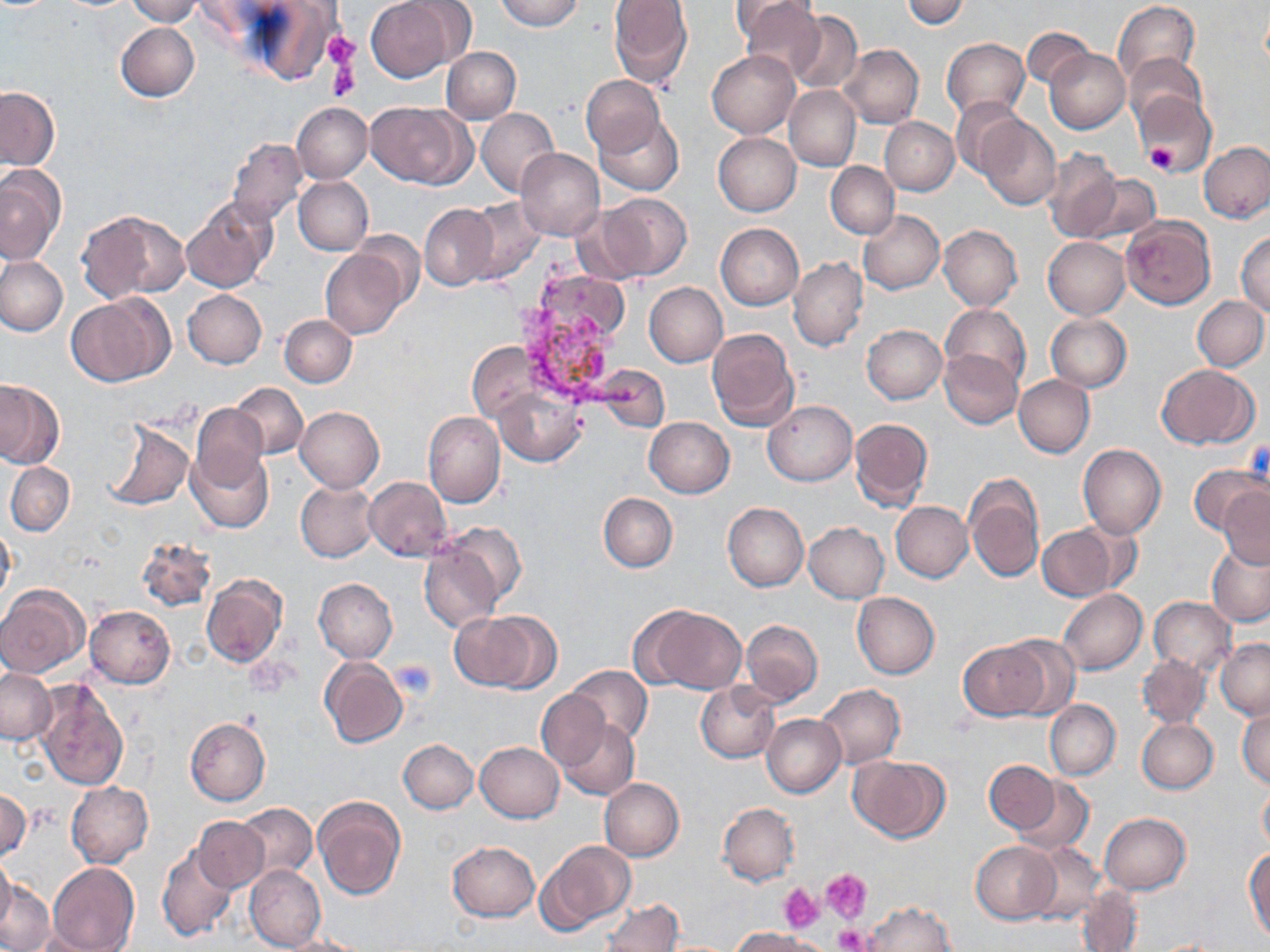

Summary:
  - Coordinate format: approximate bounding boxes as [x1, y1, x2, y2] in pixels
  - Platelet locations: [322, 32, 358, 70], [326, 52, 361, 102], [1146, 140, 1177, 175], [391, 661, 437, 699], [820, 869, 871, 923], [780, 883, 824, 933], [835, 925, 871, 952]
  - Uninfected red blood cell locations: [127, 0, 200, 26], [369, 0, 461, 81], [496, 0, 584, 31], [608, 0, 694, 88], [899, 0, 970, 29], [737, 1, 825, 82], [1113, 1, 1200, 86], [243, 2, 340, 86], [788, 9, 863, 94], [116, 22, 198, 101], [1021, 29, 1093, 89], [942, 37, 1029, 119], [839, 44, 924, 128], [441, 47, 520, 123], [1045, 49, 1129, 133], [707, 50, 798, 139], [1124, 54, 1206, 131], [581, 76, 664, 155], [784, 85, 861, 172], [0, 88, 58, 169], [1132, 92, 1215, 177], [952, 96, 1025, 178], [292, 102, 371, 183], [366, 102, 469, 188], [476, 107, 560, 197], [595, 115, 683, 197], [978, 116, 1060, 210], [880, 117, 958, 195], [714, 133, 801, 217], [226, 137, 307, 227], [1198, 141, 1270, 224], [516, 148, 605, 242], [1041, 150, 1123, 242], [826, 162, 899, 239], [830, 162, 928, 286], [0, 164, 66, 264], [1078, 172, 1161, 244], [294, 177, 373, 255], [598, 193, 692, 280], [182, 196, 277, 293], [464, 198, 547, 283], [420, 204, 500, 291], [858, 210, 944, 294], [79, 211, 189, 301], [1120, 215, 1215, 309], [715, 223, 804, 310], [938, 224, 1022, 311], [1236, 229, 1270, 316], [1042, 237, 1131, 318], [321, 248, 409, 339], [0, 256, 67, 335], [788, 257, 868, 351], [644, 282, 727, 366], [184, 290, 266, 368], [66, 294, 170, 386], [1193, 295, 1269, 371], [941, 304, 1030, 388], [1045, 314, 1131, 391], [279, 315, 356, 387], [862, 324, 947, 404], [707, 327, 799, 430], [469, 343, 537, 420], [938, 349, 1022, 428], [591, 362, 674, 434], [1158, 365, 1257, 448], [1013, 375, 1094, 458], [0, 378, 64, 468], [232, 382, 308, 459], [495, 387, 585, 467], [764, 401, 857, 485], [191, 403, 268, 488], [295, 406, 384, 494], [424, 412, 505, 508], [644, 416, 734, 497], [850, 418, 932, 510], [102, 419, 193, 511], [1079, 444, 1166, 539], [187, 447, 274, 532], [5, 462, 74, 536], [1189, 464, 1267, 536], [963, 473, 1044, 582], [364, 477, 452, 562], [296, 480, 379, 562], [1219, 488, 1270, 569], [599, 493, 677, 572], [723, 502, 808, 591], [891, 502, 972, 582], [0, 521, 14, 609], [444, 521, 524, 603], [804, 522, 888, 602], [1038, 524, 1120, 602], [136, 536, 215, 612], [419, 539, 506, 632], [1207, 542, 1270, 627], [201, 575, 287, 669], [314, 578, 397, 663], [0, 587, 87, 677], [1058, 589, 1147, 674], [852, 592, 939, 679], [1149, 597, 1235, 672], [86, 606, 175, 688], [639, 606, 748, 695], [463, 610, 561, 695], [740, 620, 823, 706], [1002, 637, 1079, 716], [1217, 639, 1270, 719], [959, 641, 1048, 720], [1137, 654, 1210, 728], [319, 657, 407, 748], [564, 665, 652, 745], [1, 668, 55, 744], [36, 679, 129, 789], [695, 682, 781, 762], [818, 684, 905, 767], [536, 689, 612, 770], [1044, 700, 1120, 779], [1238, 703, 1270, 790], [761, 714, 846, 797], [185, 717, 270, 805], [557, 719, 641, 801], [1137, 719, 1219, 793], [398, 739, 478, 813], [475, 742, 563, 822], [849, 756, 948, 842], [986, 760, 1059, 834], [1011, 776, 1094, 854], [598, 778, 684, 861], [1257, 778, 1270, 854], [67, 781, 153, 868], [0, 790, 30, 862], [314, 796, 405, 900], [234, 803, 317, 880], [718, 803, 798, 885], [1101, 813, 1190, 894], [194, 816, 270, 890], [538, 841, 635, 931], [971, 841, 1061, 923], [448, 842, 540, 922], [157, 844, 238, 942], [1028, 844, 1105, 925], [1245, 850, 1270, 942], [0, 855, 15, 933], [47, 863, 139, 952], [244, 865, 325, 951], [0, 880, 54, 952], [1076, 889, 1142, 951], [601, 900, 682, 952], [865, 901, 956, 952], [732, 927, 826, 951], [22, 928, 112, 951], [276, 934, 363, 952]
  - Slide-level diagnosis: Plasmodium vivax
  - Image size: 1270×952 pixels
  - Modality: light microscopy
  - Preparation: thin blood smear
  - Field of view: one of a larger specimen
  - Stain: May-Grünwald-Giemsa
  - Magnification: 1000x